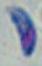

Summary:
  - Modality: micrograph
  - Magnification: 1000x
  - Identification: Toxoplasma gondii